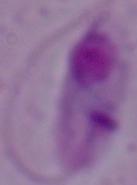
Summary:
  - Modality: photomicrograph
  - Magnification: 1000x
  - Identification: Leishmania